Report the malaria status of this cell.
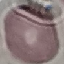

It is uninfected.

Summary:
  - Capture: smartphone through the microscope eyepiece
  - Preparation: thin blood film
  - Stain: Giemsa
  - Image type: cell patch, automatically extracted from a larger field of view and resized to 64 × 64 pixels